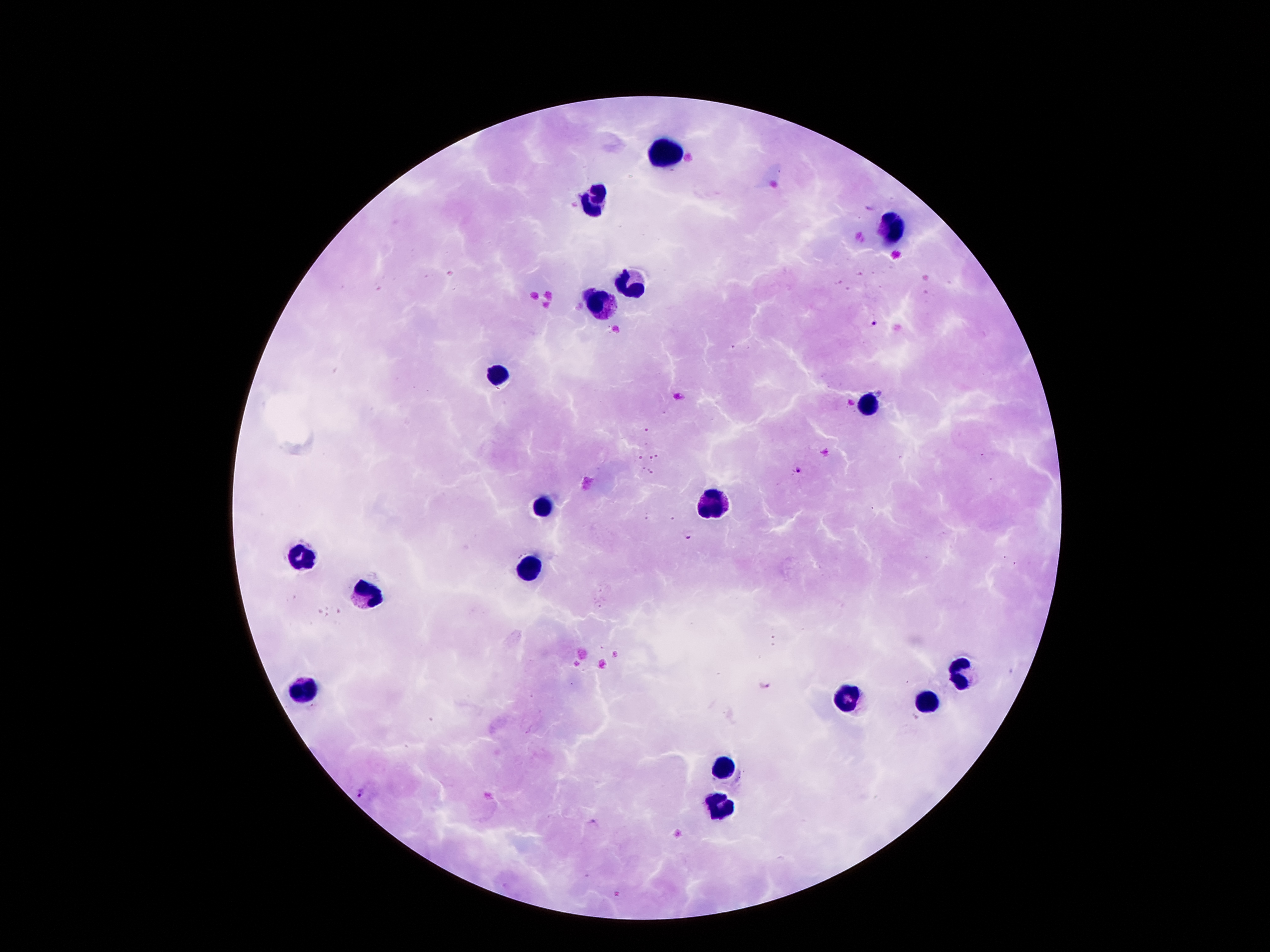

field_of_view: one from this slide
malaria_parasite_locations: 'approximate centers as [x, y] in pixels: [873, 322], [798, 470], [689, 534], [764, 683], [360, 793], [593, 824]'
preparation: thick blood film
stain: Giemsa
capture: smartphone camera through the microscope eyepiece
leukocyte_locations: 'approximate centers as [x, y] in pixels: [666, 148], [592, 197], [890, 228], [630, 285], [601, 304], [498, 375], [867, 409], [710, 501], [544, 509], [300, 553], [531, 568], [370, 595], [962, 673], [305, 690], [846, 700], [928, 702], [722, 763], [718, 810]'
magnification: 100x
image_size: 1270×952 pixels
patient_malaria_status: infected with Plasmodium falciparum